Identify the blood parasite species.
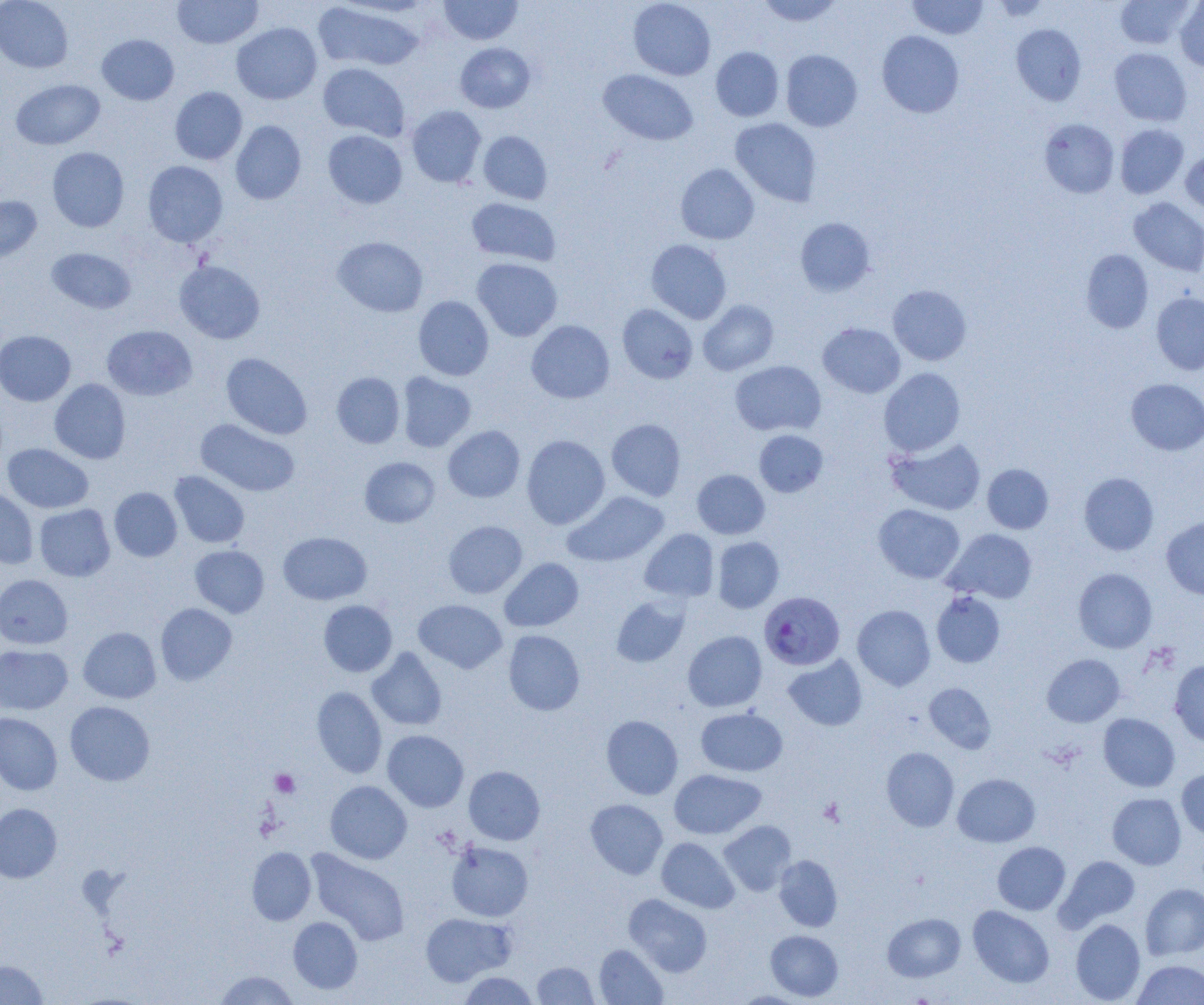

Plasmodium falciparum.

Summary:
  - Coordinate format: approximate bounding boxes as [x1, y1, x2, y2] in pixels
  - Platelet locations: [270, 769, 300, 797], [818, 797, 845, 826]
  - Uninfected red blood cell locations: [0, 0, 73, 73], [172, 0, 263, 49], [438, 0, 523, 45], [628, 0, 716, 80], [756, 0, 843, 26], [907, 0, 988, 39], [1115, 0, 1196, 49], [312, 2, 425, 72], [1175, 2, 1204, 71], [231, 22, 322, 104], [1011, 24, 1086, 105], [877, 31, 964, 118], [97, 34, 179, 105], [455, 42, 536, 113], [711, 47, 784, 121], [1109, 47, 1192, 125], [781, 49, 862, 132], [317, 63, 410, 141], [598, 69, 698, 146], [11, 79, 105, 149], [170, 86, 247, 164], [407, 106, 486, 187], [730, 118, 821, 206], [1039, 118, 1120, 198], [230, 121, 306, 205], [1115, 124, 1189, 199], [1125, 124, 1195, 274], [323, 130, 407, 208], [478, 131, 553, 204], [47, 147, 129, 232], [1180, 151, 1204, 214], [143, 161, 228, 247], [675, 164, 759, 244], [0, 195, 41, 264], [466, 198, 560, 266], [1129, 198, 1204, 275], [795, 217, 876, 296], [333, 236, 428, 317], [646, 239, 732, 324], [46, 247, 137, 314], [1081, 249, 1154, 333], [472, 258, 563, 341], [174, 260, 265, 344], [888, 284, 971, 365], [1151, 292, 1204, 375], [414, 296, 494, 381], [698, 300, 778, 376], [617, 304, 698, 384], [526, 320, 615, 404], [818, 323, 905, 398], [102, 325, 197, 400], [0, 330, 76, 406], [221, 353, 312, 440], [730, 360, 826, 436], [878, 367, 965, 456], [332, 372, 405, 448], [397, 372, 476, 452], [1126, 378, 1204, 455], [50, 379, 131, 464], [196, 418, 301, 497], [606, 419, 686, 500], [443, 426, 525, 502], [754, 429, 828, 497], [521, 435, 610, 529], [886, 436, 986, 515], [3, 443, 93, 513], [360, 456, 440, 528], [982, 463, 1054, 534], [692, 469, 770, 539], [170, 471, 250, 548], [1078, 472, 1159, 555], [0, 487, 38, 569], [109, 487, 182, 562], [563, 491, 668, 567], [34, 504, 115, 581], [873, 504, 965, 583], [1161, 517, 1204, 600], [443, 520, 527, 598], [640, 529, 719, 603], [944, 529, 1038, 603], [278, 531, 372, 605], [712, 537, 784, 613], [190, 545, 269, 618], [500, 558, 584, 631], [1073, 568, 1157, 653], [0, 574, 72, 649], [931, 590, 1005, 667], [611, 595, 690, 667], [414, 599, 507, 673], [318, 600, 397, 677], [155, 603, 237, 685], [852, 605, 935, 690], [78, 627, 161, 703], [503, 630, 585, 716], [683, 631, 767, 711], [0, 645, 73, 714], [366, 647, 447, 731], [1042, 653, 1125, 727], [783, 655, 867, 731], [1169, 660, 1204, 746], [924, 682, 996, 753], [311, 686, 387, 778], [65, 701, 155, 786], [696, 707, 787, 777], [0, 712, 63, 795], [1098, 713, 1180, 792], [601, 715, 683, 800], [382, 730, 469, 812], [881, 747, 959, 831], [463, 766, 545, 845], [1176, 768, 1204, 840], [669, 769, 766, 839], [953, 773, 1041, 847], [325, 780, 412, 864], [1107, 792, 1186, 869], [585, 799, 668, 879], [0, 803, 61, 883], [719, 820, 796, 896], [657, 837, 739, 913], [446, 841, 533, 921], [992, 842, 1070, 914], [247, 847, 316, 925], [306, 849, 410, 945], [774, 855, 842, 931], [1057, 856, 1140, 930], [1141, 883, 1204, 960], [623, 894, 712, 976], [968, 905, 1054, 988], [882, 912, 965, 982], [420, 913, 515, 986], [288, 917, 362, 994], [1071, 919, 1145, 1004], [765, 930, 843, 1001], [594, 944, 667, 1004], [1132, 959, 1204, 1004], [0, 960, 47, 1005], [532, 961, 598, 1004], [213, 971, 300, 1004], [458, 971, 539, 1004], [729, 990, 812, 1004]
  - Plasmodium falciparum-infected red blood cell locations: [759, 591, 845, 670]
  - Modality: light microscopy
  - Field of view: single
  - Magnification: 1000x
  - Preparation: thin blood smear
  - Image size: 1204×1005 pixels